Identify the parasite.
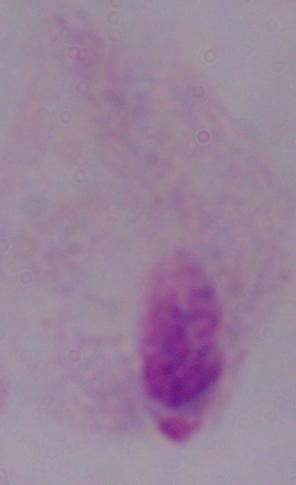
This is a trichomonad.

Photomicrograph. Captured at 1000x magnification.